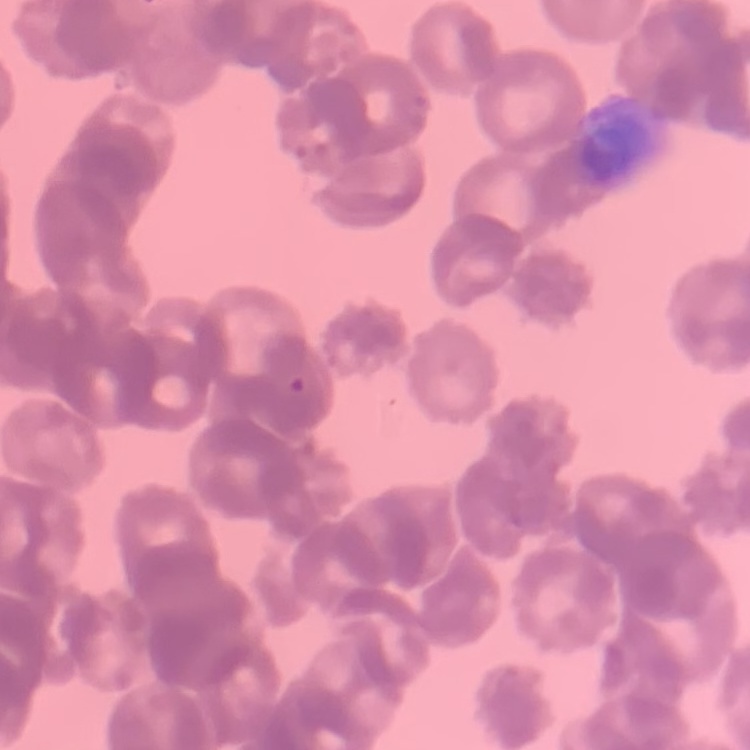
{
  "red_blood_cell_morphology": "rouleaux formation",
  "preparation": "thin peripheral smear",
  "stain": "Field's or Giemsa",
  "image_type": "square crop of a larger photomicrograph"
}